Locate platelets.
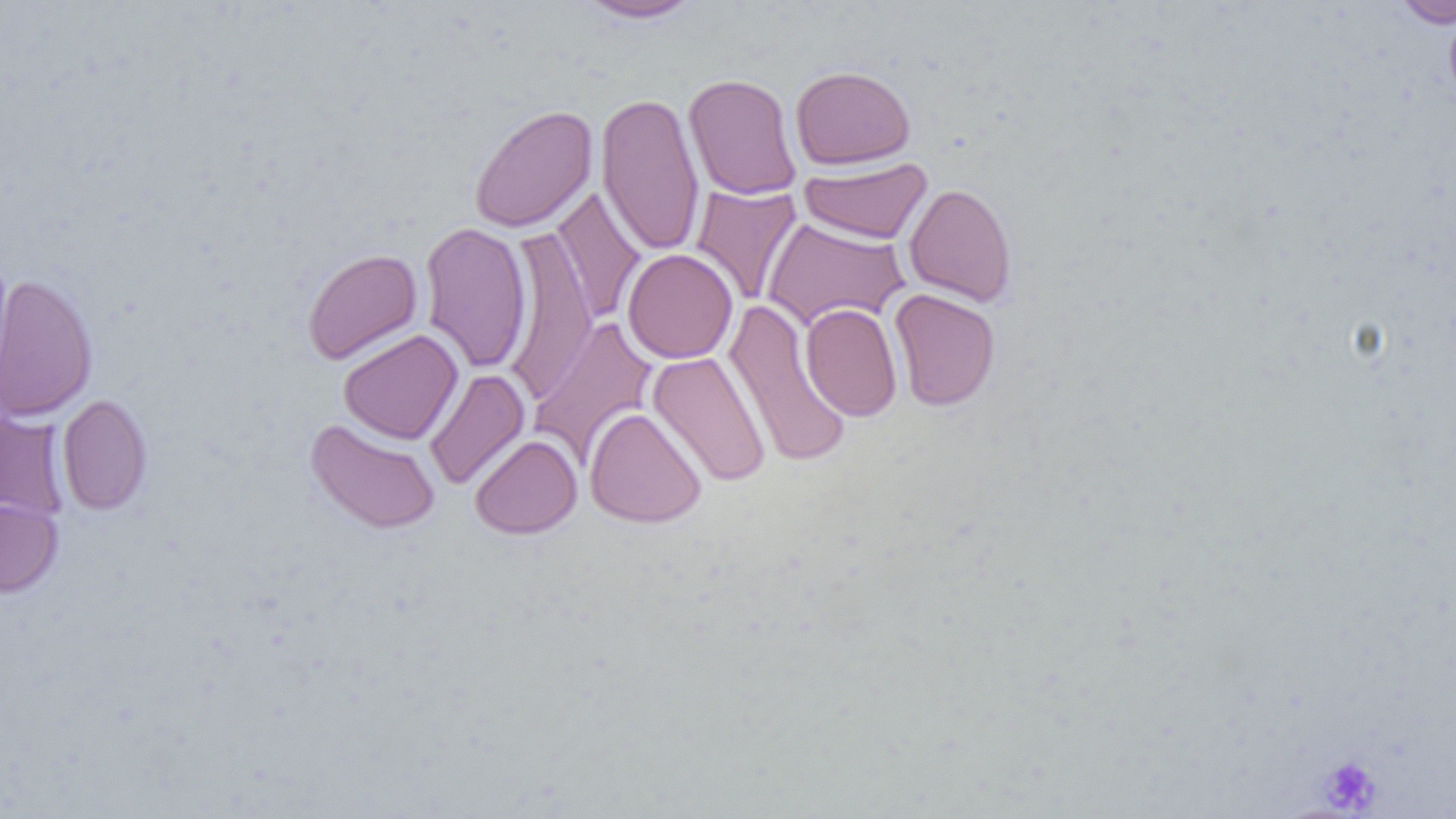
Approximate bounding boxes as [x1, y1, x2, y2] in pixels.
Platelets: [1317, 754, 1383, 814].

slide-level diagnosis = no evidence of blood parasites
image size = 1456×819 pixels
field of view = one of a larger specimen
modality = optical microscopy
uninfected red blood cell locations = approximate bounding boxes as [x1, y1, x2, y2] in pixels: [575, 0, 706, 23], [1387, 0, 1456, 28], [790, 65, 916, 169], [683, 73, 801, 200], [596, 91, 705, 257], [469, 104, 598, 234], [799, 156, 933, 245], [904, 182, 1017, 307], [691, 183, 803, 307], [549, 186, 646, 325], [762, 216, 910, 331], [420, 221, 532, 374], [502, 227, 598, 403], [302, 248, 422, 365], [622, 248, 738, 364], [0, 273, 98, 422], [888, 288, 1001, 411], [722, 298, 853, 469], [801, 302, 902, 422], [529, 316, 658, 468], [338, 329, 463, 444], [647, 351, 771, 488], [424, 369, 529, 491], [57, 394, 152, 515], [584, 406, 707, 528], [0, 410, 70, 522], [305, 418, 441, 535], [469, 434, 582, 539], [0, 498, 63, 598]
preparation = thin blood smear
magnification = 1000x